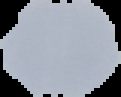
Malaria status: uninfected. From a thin blood smear. Segmented cell region on a black background. Image is 121×97 pixels.